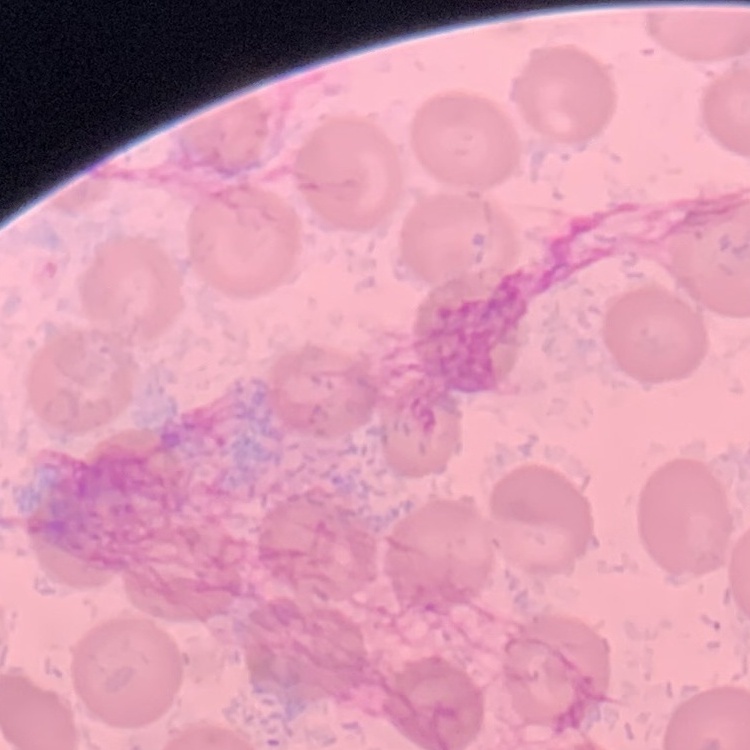

The red blood cells show no rouleaux formation. Thin peripheral smear. Square crop of a larger photomicrograph. Stained with either Field's or Giemsa.